Classify this cell by malaria status.
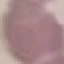
Uninfected.

Thin blood film. Automatically extracted cell patch, resized to 64 × 64 pixels. Acquired by smartphone through the microscope eyepiece. Giemsa-stained preparation.